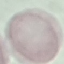
Summary:
  - Malaria status: uninfected
  - Capture: smartphone camera at the microscope eyepiece
  - Stain: Giemsa
  - Image type: cell patch, automatically extracted from a larger field of view and resized to 64 × 64 pixels
  - Preparation: thin blood smear